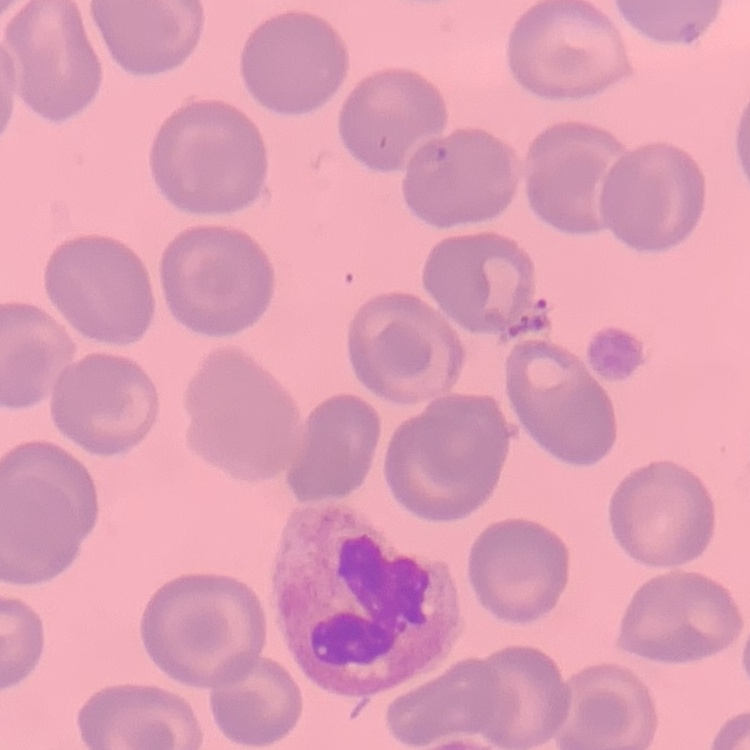

Summary:
  - Erythrocyte morphology: no rouleaux formation
  - Preparation: thin blood film
  - Image type: square crop of a larger photomicrograph
  - Stain: Field's or Giemsa